Assess the morphology of the erythrocytes.
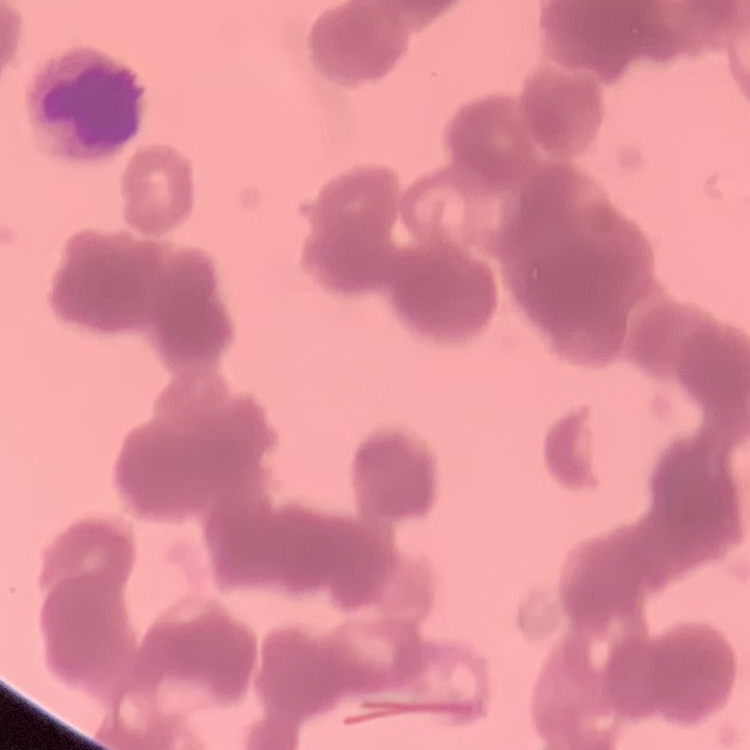
They show rouleaux formation.

Thin blood smear. One tile cut from a larger photomicrograph. Field's or Giemsa stain.